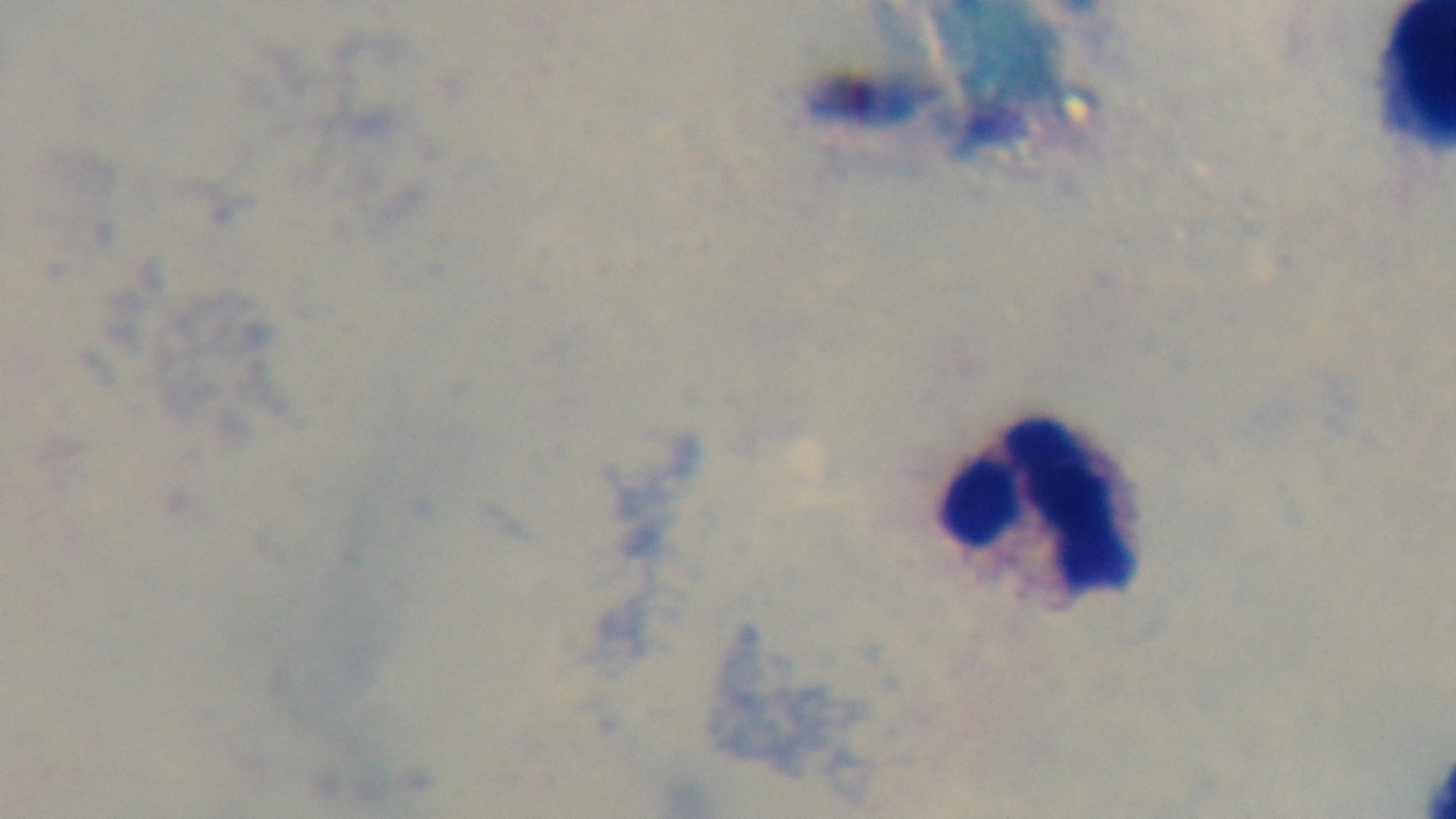

modality = light microscopy
preparation = thick
field of view = single
objective = 100x oil immersion
stain = Giemsa
malaria status = uninfected
capture = mounted 4K digital camera